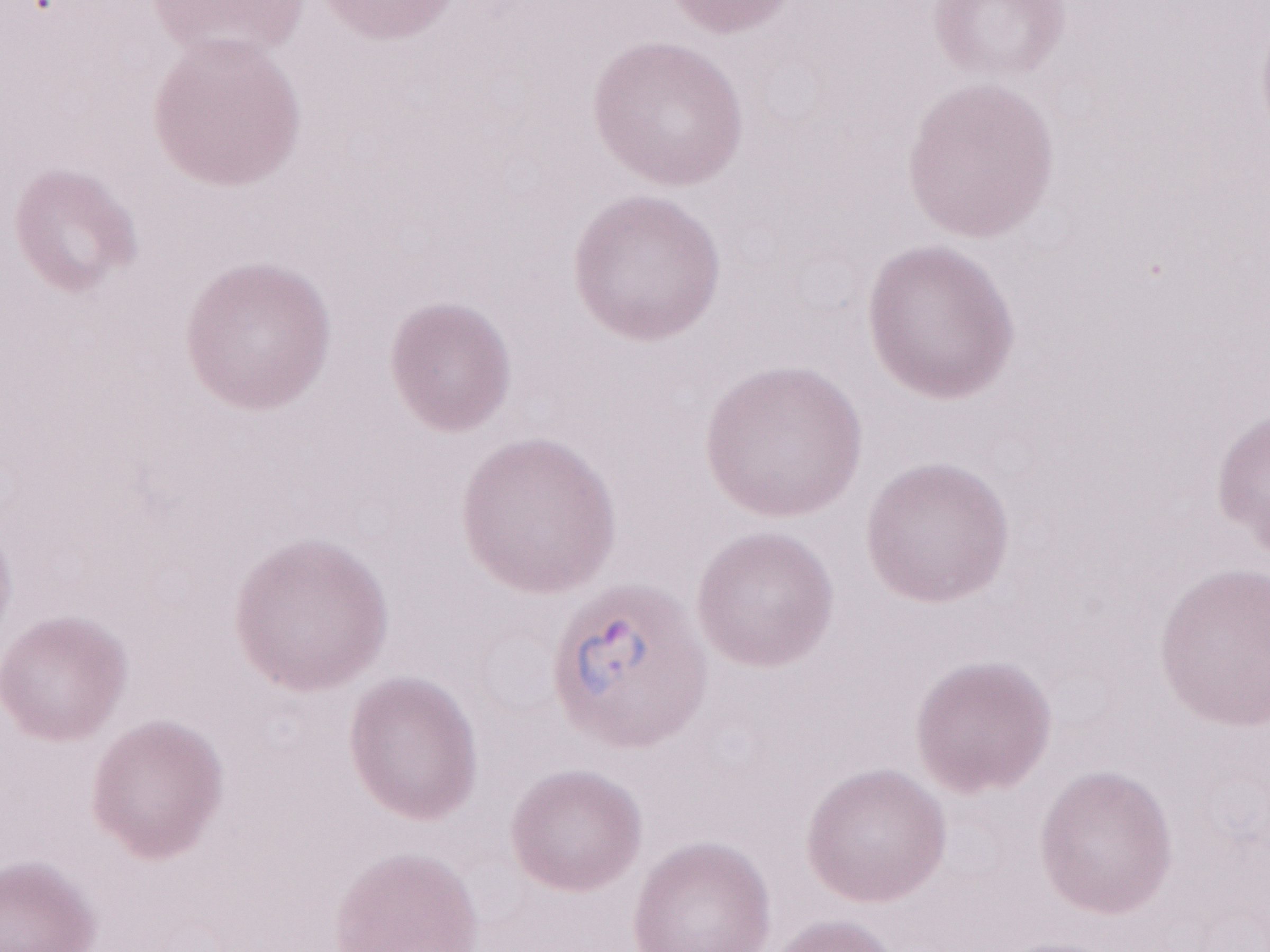 Thin blood smear. May-Grünwald-Giemsa (MGG) stain. Olympus BX43 microscope and DP73 digital camera. One field of this slide. Image is 1270×952 pixels. 1,000x magnification. Patient diagnosis: malaria infection.